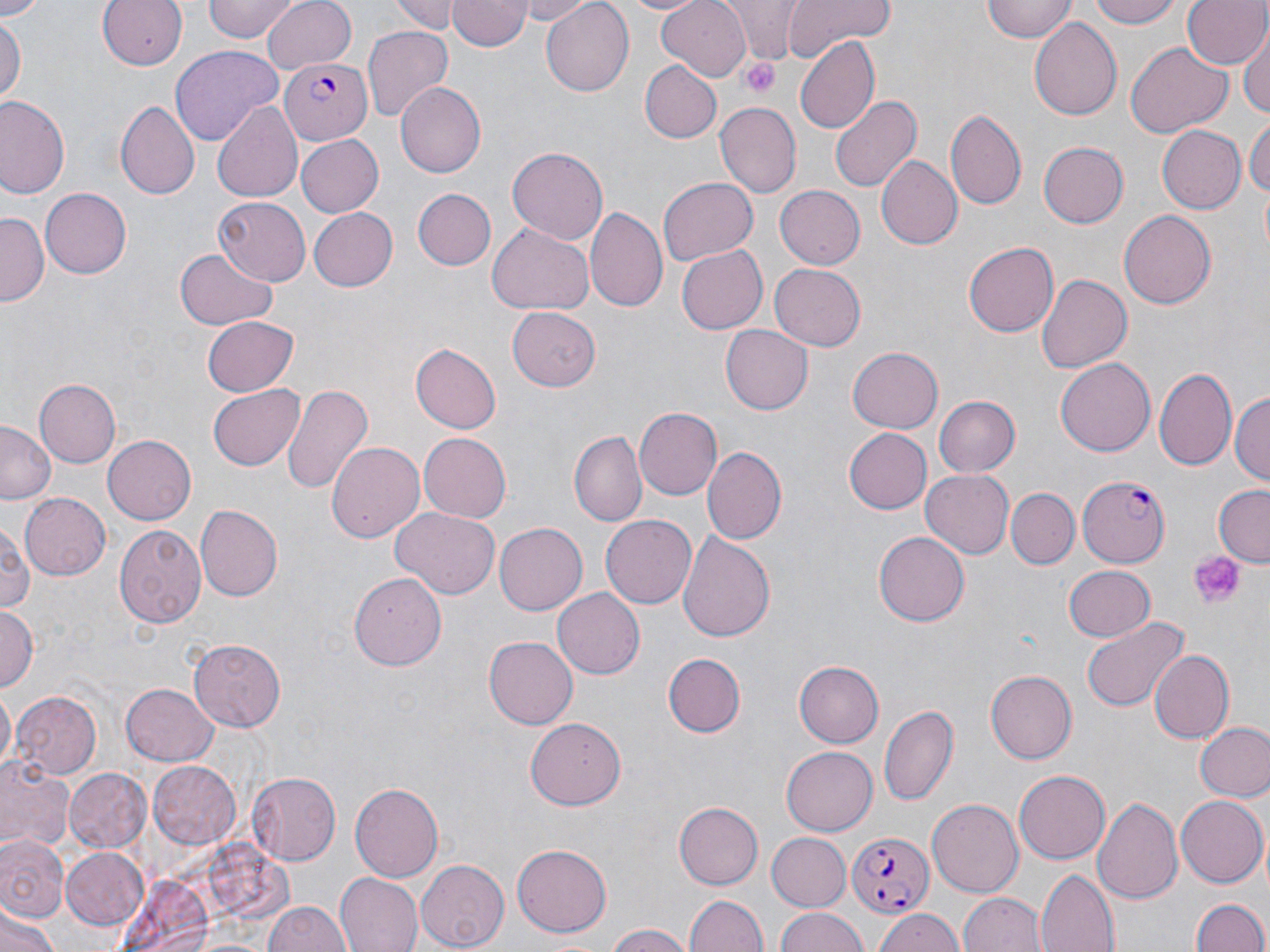
Approximate bounding boxes as (x1, y1, x2, y2) in pixels. Plasmodium falciparum-infected red blood cell locations: (280, 56, 371, 144), (1077, 474, 1170, 566), (847, 833, 933, 918). Platelet locations: (740, 56, 783, 97), (1188, 552, 1242, 608). Uninfected red blood cell locations: (0, 0, 47, 18), (99, 0, 187, 71), (202, 0, 300, 43), (262, 0, 357, 73), (394, 0, 463, 33), (448, 0, 531, 51), (511, 0, 594, 24), (619, 0, 704, 15), (656, 0, 754, 83), (785, 0, 894, 56), (981, 0, 1078, 43), (1092, 0, 1183, 26), (1183, 0, 1268, 72), (540, 1, 634, 95), (722, 1, 809, 61), (0, 15, 24, 109), (1028, 18, 1122, 119), (363, 25, 453, 121), (1241, 28, 1269, 117), (795, 35, 879, 137), (1126, 42, 1231, 138), (170, 45, 284, 145), (638, 61, 720, 143), (395, 82, 486, 178), (830, 94, 922, 192), (0, 97, 71, 201), (116, 100, 201, 200), (213, 100, 302, 204), (713, 104, 800, 198), (946, 106, 1026, 211), (1246, 115, 1269, 203), (1154, 125, 1245, 214), (295, 134, 384, 218), (1038, 141, 1128, 228), (507, 147, 608, 245), (875, 155, 963, 250), (659, 176, 758, 266), (39, 187, 132, 280), (774, 187, 863, 268), (412, 188, 496, 270), (213, 196, 310, 283), (307, 207, 397, 291), (585, 207, 669, 314), (1120, 211, 1216, 309), (0, 214, 47, 305), (488, 224, 594, 314), (964, 241, 1059, 336), (676, 245, 767, 334), (175, 248, 277, 330), (768, 264, 866, 351), (1037, 274, 1131, 373), (508, 307, 602, 392), (200, 316, 298, 395), (721, 325, 813, 413), (409, 342, 501, 432), (847, 347, 943, 434), (1055, 358, 1155, 457), (1154, 366, 1236, 470), (34, 378, 121, 467), (282, 382, 374, 499), (207, 384, 305, 470), (1231, 391, 1269, 490), (932, 395, 1020, 477), (633, 406, 722, 500), (0, 423, 58, 503), (843, 427, 933, 514), (571, 432, 644, 524), (419, 433, 512, 521), (103, 436, 196, 523), (325, 441, 424, 544), (703, 447, 786, 544), (921, 468, 1015, 559), (1212, 486, 1270, 565), (1007, 488, 1079, 569), (19, 493, 110, 581), (196, 504, 282, 599), (391, 507, 501, 600), (601, 514, 698, 609), (0, 520, 36, 617), (494, 522, 587, 616), (117, 524, 208, 628), (675, 529, 776, 643), (875, 530, 972, 625), (1062, 565, 1154, 642), (349, 574, 449, 671), (551, 588, 644, 680), (0, 603, 38, 694), (1082, 618, 1188, 712), (483, 636, 577, 729), (188, 639, 287, 732), (1148, 649, 1234, 743), (663, 652, 747, 736), (794, 661, 883, 747), (985, 668, 1077, 763), (121, 683, 217, 764), (1, 687, 14, 772), (12, 692, 101, 780), (880, 702, 959, 807), (526, 717, 626, 809), (1194, 720, 1270, 803), (781, 746, 876, 836), (0, 757, 72, 854), (148, 761, 243, 849), (64, 767, 150, 853), (1014, 768, 1111, 864), (246, 771, 340, 865), (351, 781, 446, 882), (1175, 795, 1266, 886), (1092, 796, 1182, 908), (927, 798, 1024, 897), (674, 801, 762, 888), (1, 833, 69, 923), (767, 833, 849, 907), (512, 844, 613, 935), (59, 847, 149, 930), (415, 861, 510, 949), (1036, 869, 1119, 951), (334, 873, 423, 952), (684, 892, 768, 952), (959, 892, 1047, 952), (1189, 896, 1270, 952), (264, 897, 351, 952), (0, 907, 60, 952), (773, 907, 870, 952), (873, 907, 964, 952), (605, 924, 691, 952). Slide-level diagnosis: Plasmodium falciparum. May-Grünwald-Giemsa stain. Image is 1270×952 pixels. Captured at 1000x magnification. Optical microscopy. Single field of view. Thin blood film.